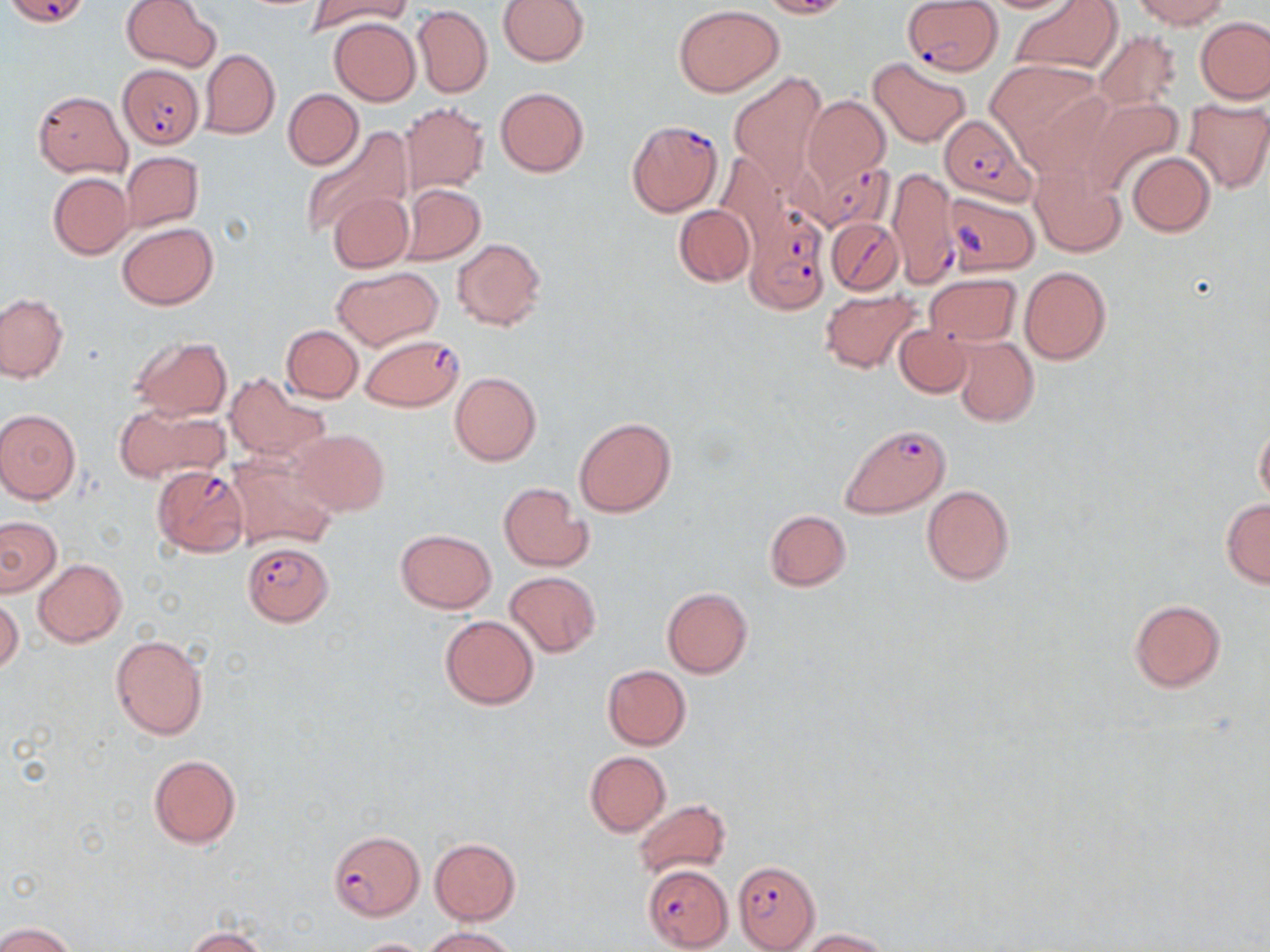
Summary:
  - Coordinate format: approximate bounding boxes as (x1,y1)-(x2,y2) corner pairs in pixels
  - Plasmodium falciparum-infected red blood cell locations: (8,0)-(89,26), (901,0)-(1002,73), (117,63)-(205,149), (938,113)-(1037,207), (625,119)-(723,216), (792,160)-(896,237), (888,169)-(959,287), (743,202)-(831,315), (827,217)-(902,296), (361,333)-(464,411), (839,424)-(950,518), (151,465)-(250,556), (244,541)-(334,626), (329,829)-(425,922), (733,861)-(822,951), (643,864)-(733,951)
  - Uninfected red blood cell locations: (122,0)-(220,71), (307,0)-(409,35), (498,0)-(590,66), (757,0)-(851,18), (980,0)-(1077,13), (1012,0)-(1122,75), (1131,0)-(1232,29), (413,5)-(492,97), (673,5)-(783,96), (1196,16)-(1269,103), (330,17)-(421,105), (1094,29)-(1182,113), (200,49)-(280,138), (869,56)-(972,148), (987,61)-(1110,169), (727,71)-(825,189), (495,86)-(589,177), (284,88)-(363,169), (34,90)-(132,177), (801,95)-(889,189), (1081,96)-(1183,194), (1183,98)-(1270,193), (400,102)-(489,195), (298,126)-(410,240), (121,151)-(203,231), (1127,152)-(1215,235), (1030,164)-(1127,258), (47,173)-(133,259), (398,183)-(486,265), (327,190)-(414,273), (674,205)-(754,286), (117,223)-(219,308), (452,238)-(547,330), (333,266)-(441,350), (1019,266)-(1112,364), (925,274)-(1022,347), (821,289)-(922,374), (0,291)-(68,383), (282,324)-(363,402), (894,324)-(972,397), (130,336)-(233,420), (953,336)-(1039,426), (450,371)-(541,465), (224,372)-(327,464), (111,406)-(222,481), (0,409)-(81,503), (573,416)-(676,518), (1254,417)-(1270,507), (290,428)-(390,516), (226,452)-(339,552), (499,482)-(595,572), (921,485)-(1015,585), (1220,499)-(1270,587), (764,509)-(852,591), (0,516)-(61,596), (396,529)-(496,613), (33,559)-(126,646), (505,571)-(600,657), (662,588)-(752,677), (0,596)-(23,675), (1129,599)-(1226,693), (439,615)-(539,709), (110,633)-(209,741), (602,664)-(691,750), (584,751)-(671,835), (148,754)-(241,850), (633,798)-(731,879), (429,838)-(522,924), (0,921)-(76,952), (422,926)-(519,952), (185,927)-(268,952), (803,929)-(890,952), (353,937)-(433,952)
  - Slide-level diagnosis: Plasmodium falciparum
  - Stain: May-Grünwald-Giemsa
  - Magnification: 1000x
  - Field of view: one of a larger specimen
  - Modality: light microscopy
  - Image size: 1270×952 pixels
  - Preparation: thin blood film